Assess the morphology of the red blood cells.
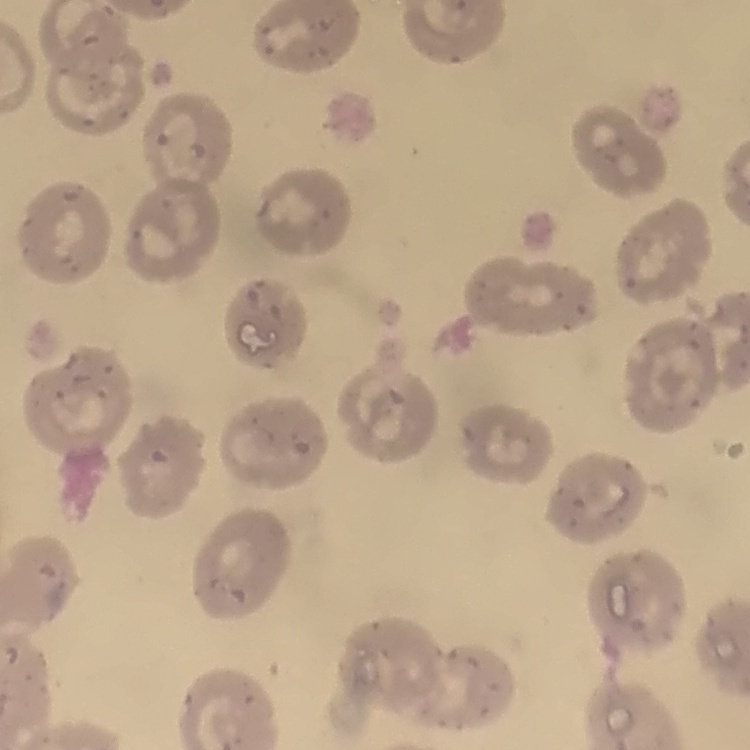
No rouleaux formation.

Summary:
  - Preparation: thin peripheral smear
  - Stain: Field's or Giemsa
  - Image type: one tile cut from a larger photomicrograph